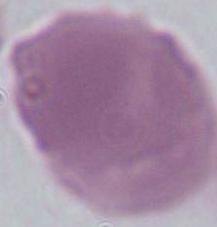
1000x magnification. An erythrocyte is seen. Photomicrograph.